Give the position of every Plasmodium parasite.
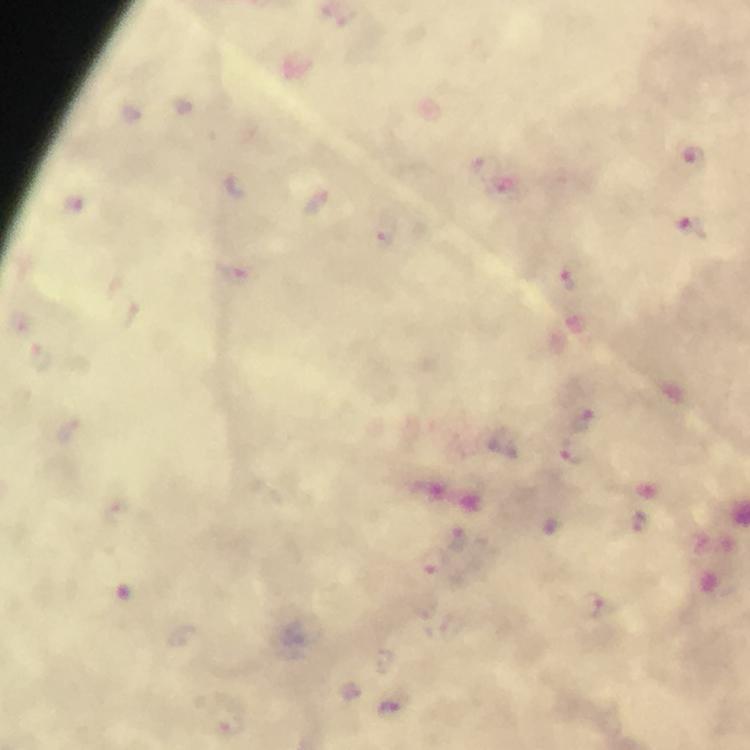
Approximate centers as [x, y] in pixels.
Plasmodium parasites: [692, 163], [487, 168], [236, 187], [319, 201], [76, 206], [694, 228], [240, 273], [571, 281], [584, 421], [578, 454], [640, 522], [457, 539], [431, 560], [591, 606], [387, 711].

context = from a malaria diagnostic workup
preparation = thick blood film
capture = smartphone mounted on the microscope
cropped from = one field of view
immersion oil = applied
image size = 750×750 pixels
magnification = 100x
stain = Giemsa